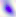

identification = Toxoplasma gondii
modality = micrograph
magnification = 400x